State the blood parasite species.
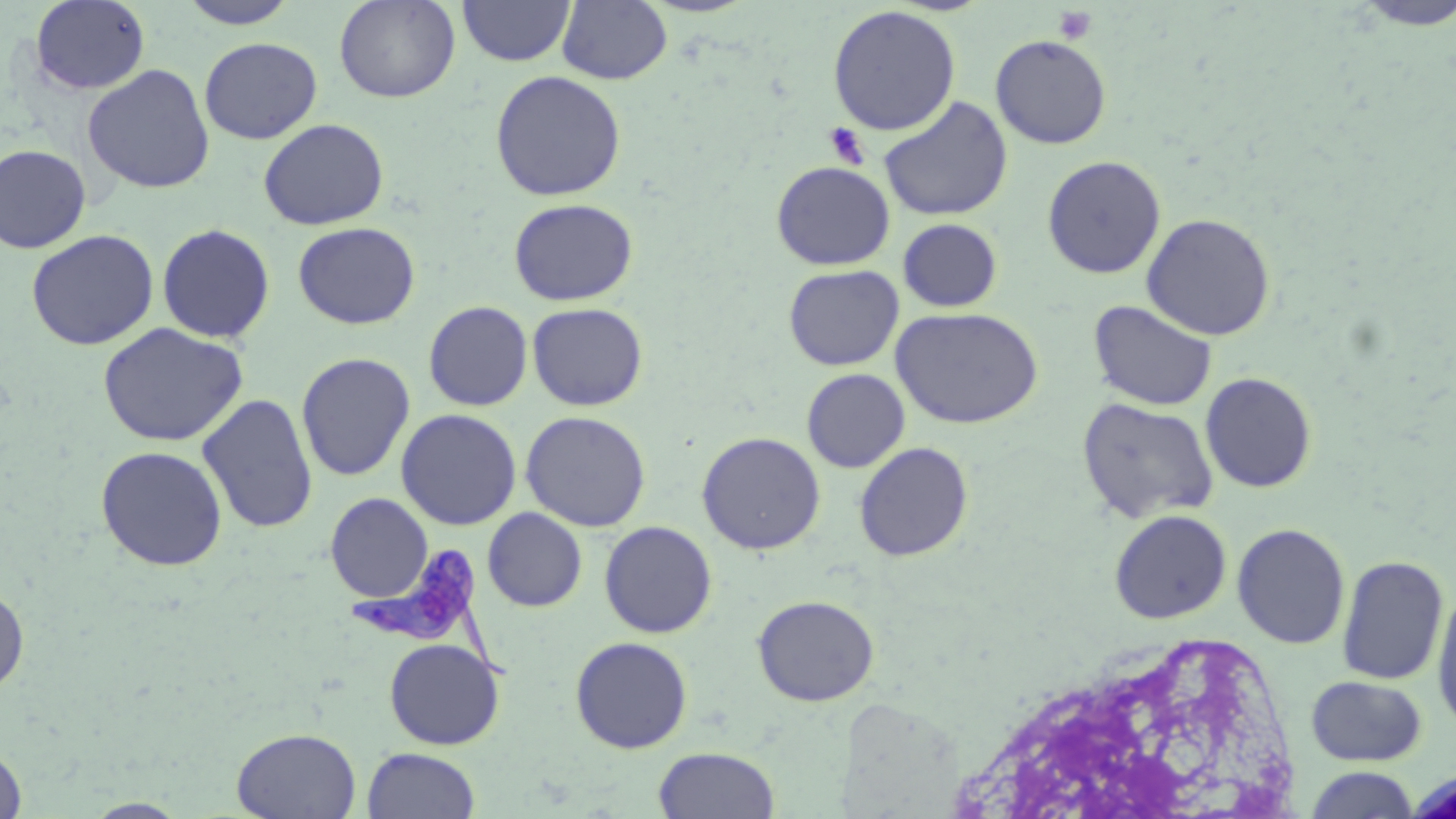
Trypanosoma brucei.

{
  "modality": "optical microscopy",
  "stain": "May-Grünwald-Giemsa",
  "platelet_locations": "approximate bounding boxes as (x1,y1)-(x2,y2) corner pairs in pixels: (1052,5)-(1096,45), (824,122)-(870,169)",
  "magnification": "1000x",
  "trypanosoma_brucei_locations": "approximate bounding boxes as (x1,y1)-(x2,y2) corner pairs in pixels: (346,547)-(512,683)",
  "field_of_view": "single",
  "image_size": "1456×819 pixels",
  "uninfected_red_blood_cell_locations": "approximate bounding boxes as (x1,y1)-(x2,y2) corner pairs in pixels: (177,0)-(300,29), (334,0)-(460,103), (457,0)-(576,67), (1347,0)-(1455,31), (29,1)-(150,95), (557,1)-(672,85), (827,5)-(962,136), (990,35)-(1111,149), (199,37)-(322,144), (82,64)-(215,194), (489,69)-(626,201), (878,96)-(1014,222), (258,118)-(389,231), (0,144)-(91,253), (1042,155)-(1166,278), (770,161)-(895,270), (508,198)-(638,306), (1141,212)-(1276,341), (897,218)-(1003,313), (293,222)-(420,329), (157,223)-(275,343), (25,229)-(160,351), (783,264)-(904,370), (1088,299)-(1218,412), (423,301)-(533,411), (527,302)-(649,411), (890,307)-(1043,429), (96,322)-(249,447), (296,352)-(415,482), (801,368)-(910,473), (1200,372)-(1317,493), (197,393)-(318,534), (1076,397)-(1219,524), (395,409)-(522,530), (520,410)-(651,532), (697,431)-(826,554), (854,442)-(973,561), (95,445)-(228,571), (325,493)-(433,602), (482,507)-(587,612), (1108,509)-(1232,624), (599,521)-(717,638), (1231,523)-(1350,649), (1336,554)-(1449,686), (0,586)-(29,696), (1431,586)-(1456,733), (752,594)-(879,706), (570,637)-(693,753), (384,638)-(505,750), (1306,676)-(1427,766), (232,727)-(360,819), (0,745)-(27,819), (361,747)-(481,819), (653,747)-(780,819), (1303,766)-(1422,818), (83,798)-(191,818)",
  "preparation": "thin blood smear"
}